Identify the preparation type.
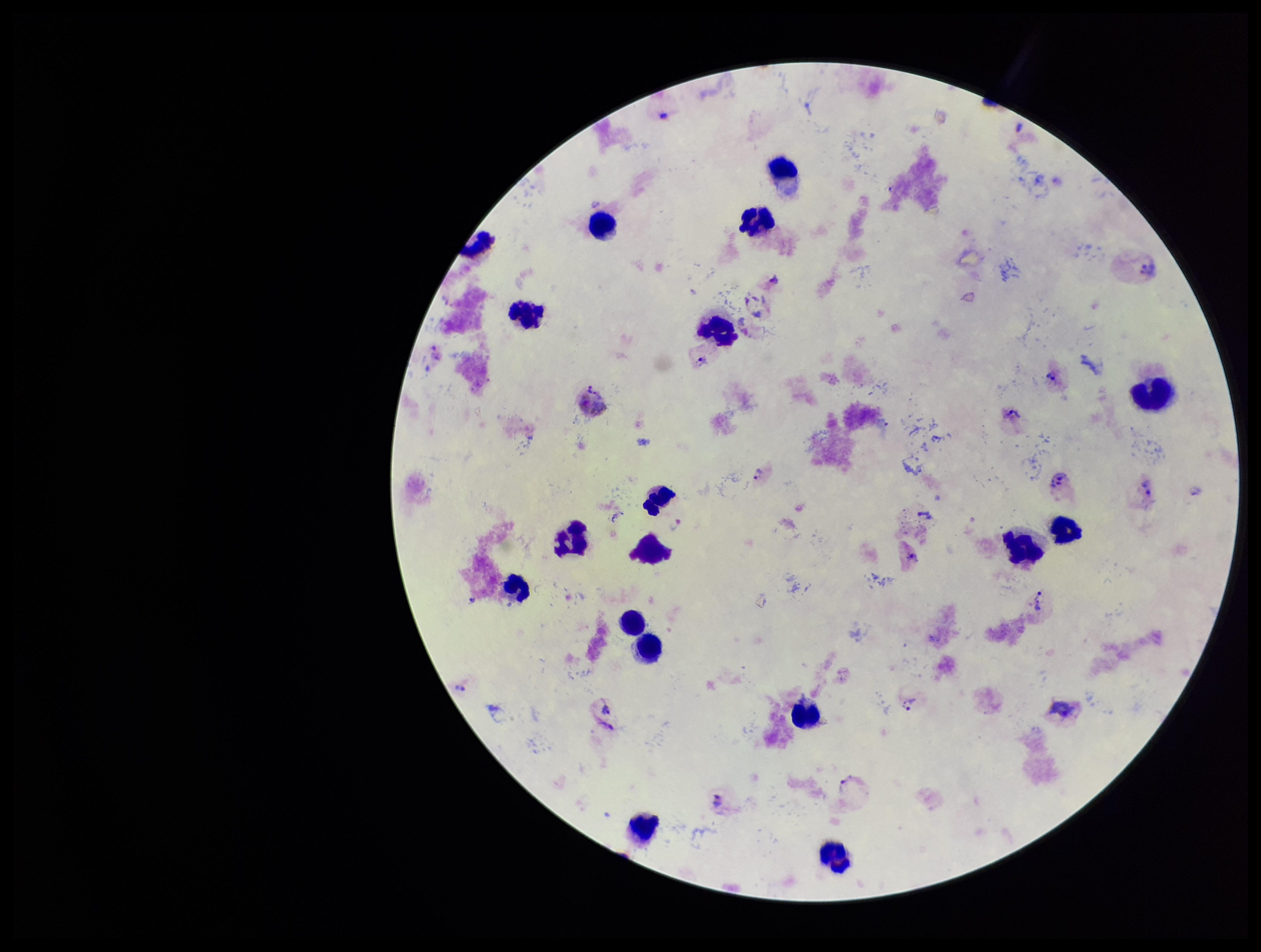

A thick smear.

Summary:
  - Plasmodium parasites: seen
  - Image size: 1261×952 pixels
  - Capture: smartphone photograph through the microscope eyepiece
  - Species reported for this patient: Plasmodium vivax
  - Stain: Giemsa
  - Patient malaria status: infected
  - Field of view: single
  - Leukocyte count: 18
  - Parasite count: 17